Outline each blood parasite and name the species.
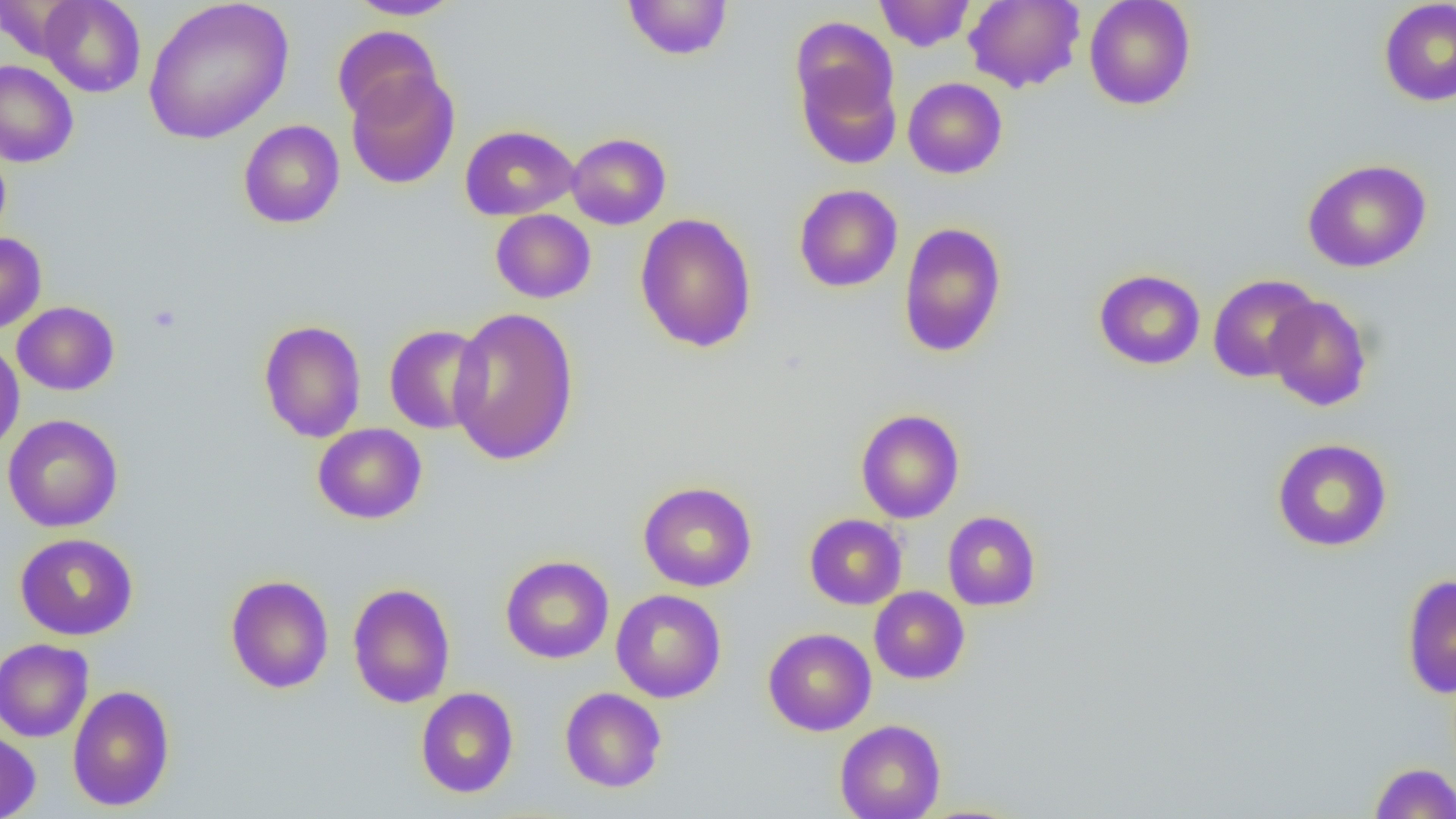
No blood parasites observed.

Approximate bounding boxes as (x1, y1, x2, y2) in pixels. Platelet locations: (148, 304, 182, 334). Uninfected red blood cell locations: (39, 0, 146, 97), (143, 0, 294, 144), (347, 0, 463, 19), (874, 0, 976, 52), (963, 0, 1085, 92), (1083, 0, 1197, 110), (1378, 0, 1456, 106), (623, 1, 732, 61), (790, 16, 899, 124), (332, 26, 442, 126), (793, 55, 901, 170), (0, 60, 79, 168), (346, 69, 460, 190), (903, 77, 1008, 178), (238, 119, 345, 229), (459, 125, 579, 221), (566, 132, 671, 230), (0, 144, 11, 245), (1303, 158, 1432, 273), (794, 184, 903, 292), (490, 209, 595, 303), (634, 213, 758, 354), (898, 221, 1007, 358), (0, 232, 47, 334), (1093, 268, 1205, 370), (1207, 274, 1320, 382), (1265, 295, 1373, 411), (12, 301, 119, 395), (447, 306, 580, 466), (258, 319, 367, 442), (384, 324, 490, 434), (0, 341, 25, 454), (855, 408, 965, 523), (3, 414, 123, 532), (313, 423, 427, 524), (1272, 438, 1392, 552), (638, 481, 757, 592), (942, 511, 1041, 611), (804, 514, 907, 609), (15, 533, 139, 641), (500, 555, 614, 664), (1401, 574, 1456, 698), (225, 575, 334, 694), (347, 582, 456, 708), (869, 586, 970, 684), (611, 589, 726, 703), (763, 627, 876, 736), (0, 638, 93, 742), (67, 685, 175, 811), (416, 687, 519, 798), (559, 687, 667, 792), (835, 720, 945, 819), (0, 728, 41, 819), (1369, 762, 1456, 818). Slide-level diagnosis: negative for blood parasites. Light microscopy. Single field of view. Thin blood smear. Image is 1456×819 pixels. Captured at 1000x magnification.